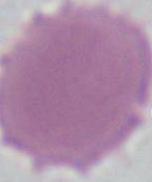

1000x magnification. Photomicrograph. A red blood cell is seen.